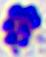
modality: micrograph
magnification: 400x
identification: leukocyte